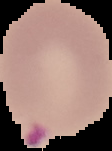

result = Plasmodium parasites detected
image size = 112×151 pixels
image type = cell region segmented out of the field of view; surrounding area masked to black
preparation = thin blood film